Describe the morphology of the red blood cells.
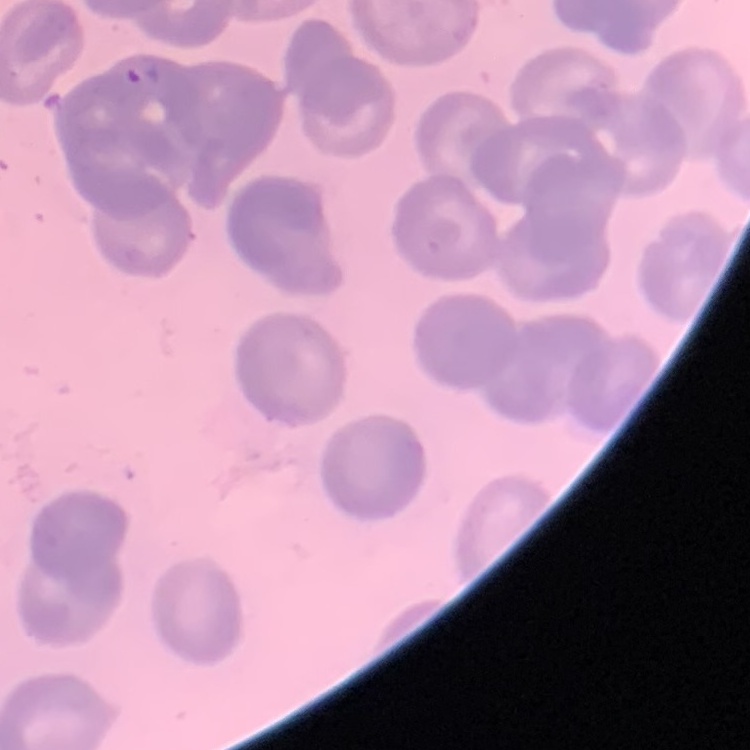

No rouleaux formation.

Square crop of a larger photomicrograph. Thin blood smear. Field's or Giemsa stain.